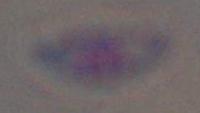
Photomicrograph. Captured at 1000x magnification. Toxoplasma gondii is shown.